Name the cell type shown.
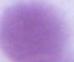
This is an erythrocyte.

Summary:
  - Magnification: 1000x
  - Modality: micrograph